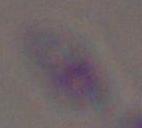

Summary:
  - Magnification: 1000x
  - Modality: micrograph
  - Identification: Toxoplasma gondii